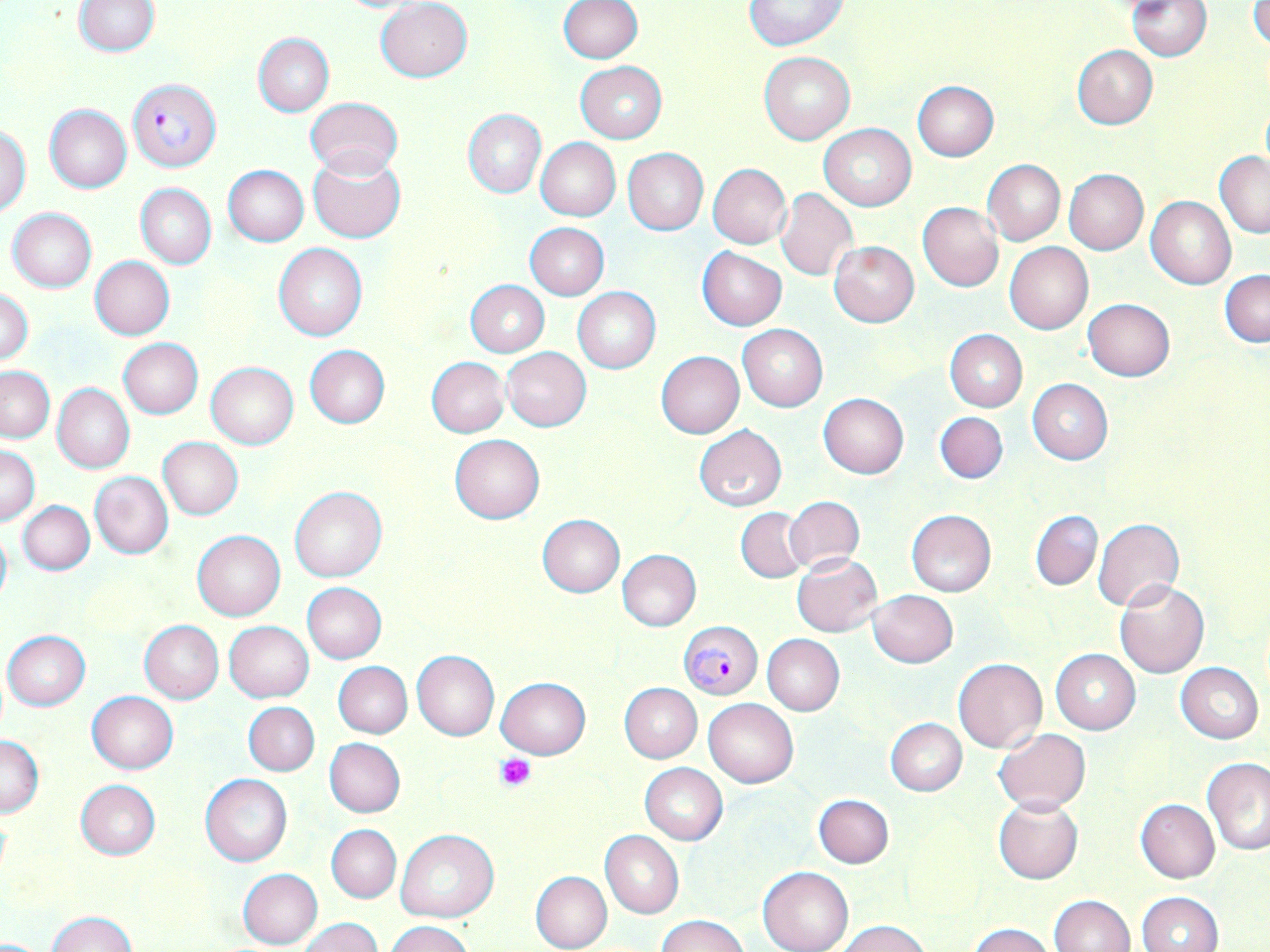 Approximate bounding boxes as named x1/y1/x2/y2 corners in pixels. Platelet locations: (x1=496, y1=754, x2=537, y2=790). Uninfected red blood cell locations: (x1=558, y1=0, x2=642, y2=63), (x1=1127, y1=0, x2=1212, y2=60), (x1=1250, y1=0, x2=1270, y2=51), (x1=73, y1=1, x2=161, y2=56), (x1=331, y1=1, x2=427, y2=13), (x1=375, y1=1, x2=472, y2=82), (x1=743, y1=1, x2=847, y2=50), (x1=253, y1=32, x2=334, y2=116), (x1=1072, y1=45, x2=1157, y2=129), (x1=759, y1=51, x2=854, y2=144), (x1=575, y1=61, x2=666, y2=142), (x1=913, y1=81, x2=999, y2=161), (x1=306, y1=97, x2=403, y2=179), (x1=44, y1=104, x2=131, y2=193), (x1=463, y1=109, x2=545, y2=198), (x1=820, y1=124, x2=916, y2=210), (x1=0, y1=126, x2=31, y2=213), (x1=536, y1=138, x2=620, y2=221), (x1=623, y1=149, x2=708, y2=233), (x1=1215, y1=151, x2=1270, y2=239), (x1=307, y1=153, x2=406, y2=244), (x1=982, y1=160, x2=1065, y2=245), (x1=709, y1=163, x2=792, y2=249), (x1=223, y1=164, x2=309, y2=246), (x1=1064, y1=169, x2=1147, y2=254), (x1=136, y1=184, x2=216, y2=269), (x1=775, y1=188, x2=857, y2=281), (x1=1146, y1=196, x2=1237, y2=289), (x1=918, y1=202, x2=1003, y2=291), (x1=7, y1=207, x2=97, y2=292), (x1=525, y1=222, x2=610, y2=300), (x1=829, y1=241, x2=919, y2=327), (x1=1005, y1=242, x2=1093, y2=334), (x1=274, y1=243, x2=366, y2=341), (x1=697, y1=247, x2=786, y2=330), (x1=90, y1=256, x2=175, y2=340), (x1=1220, y1=269, x2=1270, y2=348), (x1=465, y1=280, x2=550, y2=357), (x1=572, y1=287, x2=661, y2=373), (x1=1, y1=289, x2=35, y2=364), (x1=1083, y1=298, x2=1176, y2=381), (x1=737, y1=324, x2=827, y2=411), (x1=945, y1=330, x2=1028, y2=411), (x1=119, y1=339, x2=202, y2=418), (x1=304, y1=345, x2=389, y2=429), (x1=502, y1=347, x2=591, y2=431), (x1=657, y1=351, x2=744, y2=438), (x1=426, y1=357, x2=510, y2=438), (x1=205, y1=363, x2=298, y2=449), (x1=1, y1=366, x2=54, y2=442), (x1=1026, y1=378, x2=1113, y2=465), (x1=52, y1=384, x2=135, y2=474), (x1=818, y1=393, x2=909, y2=478), (x1=934, y1=411, x2=1008, y2=484), (x1=693, y1=424, x2=787, y2=510), (x1=449, y1=434, x2=544, y2=524), (x1=157, y1=438, x2=243, y2=520), (x1=1, y1=446, x2=39, y2=526), (x1=89, y1=471, x2=173, y2=559), (x1=290, y1=487, x2=385, y2=582), (x1=783, y1=496, x2=865, y2=575), (x1=17, y1=501, x2=95, y2=575), (x1=735, y1=505, x2=809, y2=583), (x1=906, y1=509, x2=996, y2=596), (x1=1031, y1=511, x2=1102, y2=590), (x1=537, y1=514, x2=625, y2=597), (x1=1092, y1=518, x2=1184, y2=613), (x1=0, y1=522, x2=12, y2=612), (x1=192, y1=530, x2=285, y2=621), (x1=616, y1=549, x2=702, y2=630), (x1=792, y1=554, x2=881, y2=636), (x1=1114, y1=580, x2=1210, y2=678), (x1=302, y1=582, x2=386, y2=663), (x1=866, y1=590, x2=958, y2=668), (x1=139, y1=620, x2=223, y2=703), (x1=224, y1=621, x2=314, y2=703), (x1=2, y1=630, x2=90, y2=710), (x1=762, y1=634, x2=845, y2=715), (x1=1051, y1=649, x2=1141, y2=734), (x1=412, y1=651, x2=498, y2=740), (x1=953, y1=657, x2=1048, y2=753), (x1=333, y1=662, x2=412, y2=739), (x1=1175, y1=662, x2=1263, y2=743), (x1=496, y1=678, x2=590, y2=759), (x1=619, y1=683, x2=702, y2=763), (x1=86, y1=691, x2=178, y2=774), (x1=703, y1=698, x2=799, y2=788), (x1=244, y1=702, x2=320, y2=775), (x1=886, y1=718, x2=967, y2=796), (x1=995, y1=728, x2=1091, y2=813), (x1=0, y1=733, x2=44, y2=819), (x1=324, y1=737, x2=406, y2=818), (x1=1202, y1=757, x2=1270, y2=854), (x1=640, y1=763, x2=728, y2=844), (x1=200, y1=774, x2=293, y2=866), (x1=74, y1=779, x2=161, y2=860), (x1=813, y1=794, x2=894, y2=868), (x1=992, y1=795, x2=1083, y2=884), (x1=1135, y1=799, x2=1220, y2=884), (x1=327, y1=825, x2=401, y2=903), (x1=902, y1=826, x2=984, y2=923), (x1=395, y1=829, x2=498, y2=922), (x1=600, y1=831, x2=683, y2=919), (x1=758, y1=867, x2=853, y2=952), (x1=238, y1=868, x2=322, y2=949), (x1=530, y1=871, x2=613, y2=952), (x1=1136, y1=892, x2=1222, y2=952), (x1=1049, y1=894, x2=1135, y2=952), (x1=49, y1=911, x2=135, y2=951), (x1=658, y1=915, x2=748, y2=952), (x1=299, y1=918, x2=383, y2=952), (x1=836, y1=919, x2=932, y2=952), (x1=388, y1=920, x2=473, y2=952), (x1=968, y1=923, x2=1058, y2=952). Plasmodium falciparum-infected red blood cell locations: (x1=129, y1=77, x2=221, y2=172), (x1=678, y1=622, x2=763, y2=699). Slide-level diagnosis: Plasmodium falciparum. Thin blood smear. Light microscopy. Image is 1270×952 pixels. Single field of view. May-Grünwald-Giemsa stain. 1000x magnification.